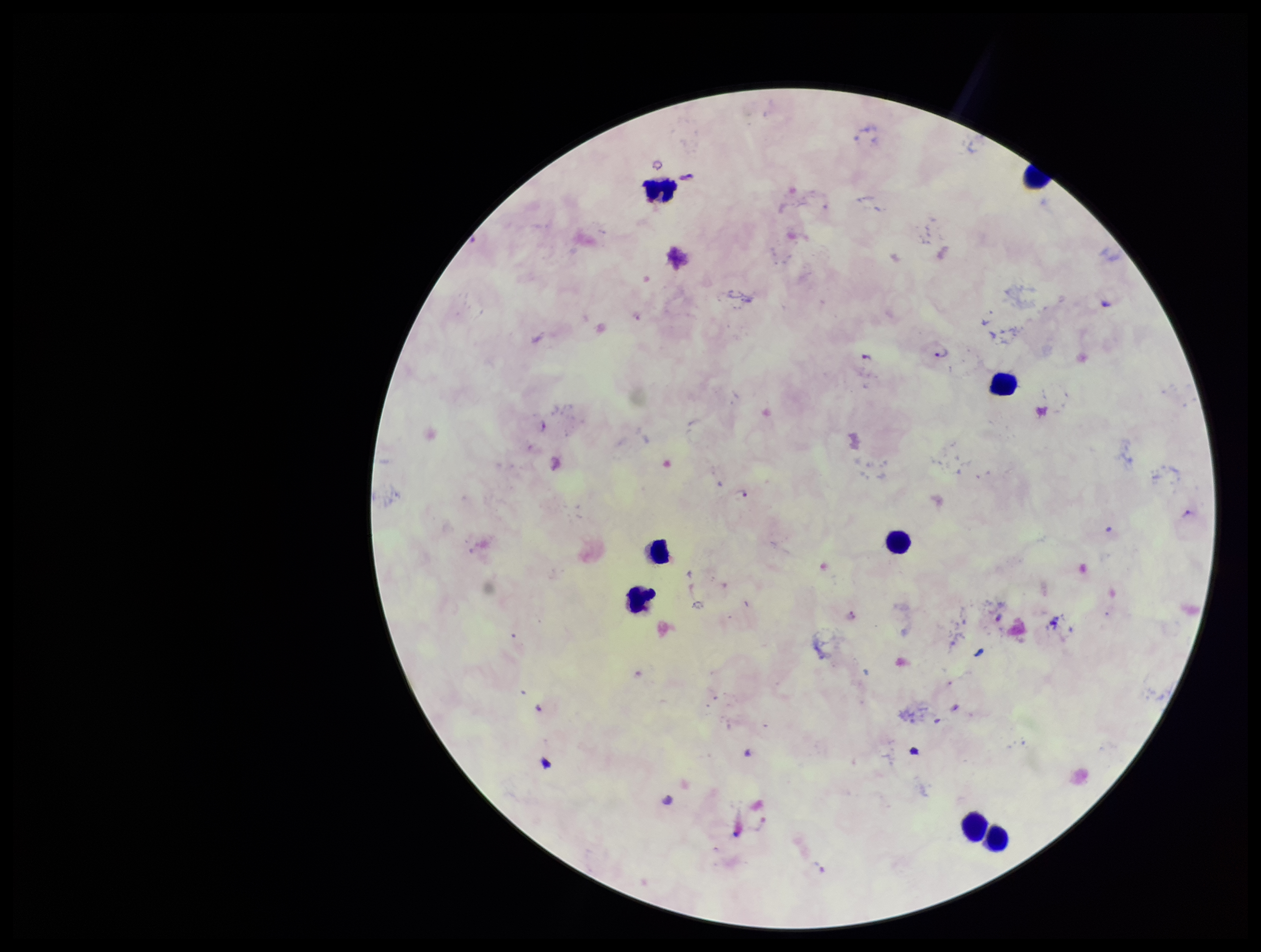

Summary:
  - Preparation: thick smear
  - Leukocyte count: 8
  - Stain: Giemsa
  - Plasmodium parasites: detected
  - Image size: 1261×952 pixels
  - Field of view: one from this slide
  - Capture: smartphone photograph through the microscope eyepiece
  - Parasite count: 7
  - Species reported for this patient: Plasmodium falciparum
  - Patient malaria status: infected